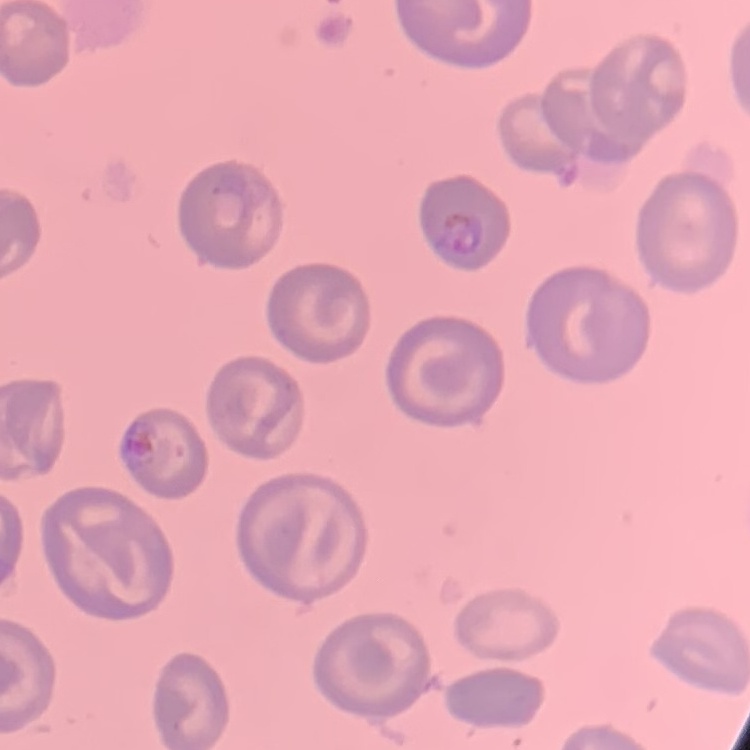
Summary:
  - Erythrocyte morphology: no rouleaux formation
  - Stain: Field's or Giemsa
  - Image type: one tile cut from a larger photomicrograph
  - Preparation: thin blood smear